State which cell type is depicted.
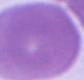

This is an erythrocyte.

Micrograph. Captured at 1000x magnification.